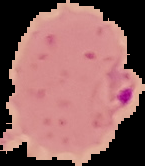
Summary:
  - Image type: segmented cell region on a black background
  - Preparation: thin blood film
  - Result: malaria parasites detected
  - Image size: 145×166 pixels